State which parasite is depicted.
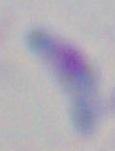
Toxoplasma gondii.

Captured at 1000x magnification. Micrograph.